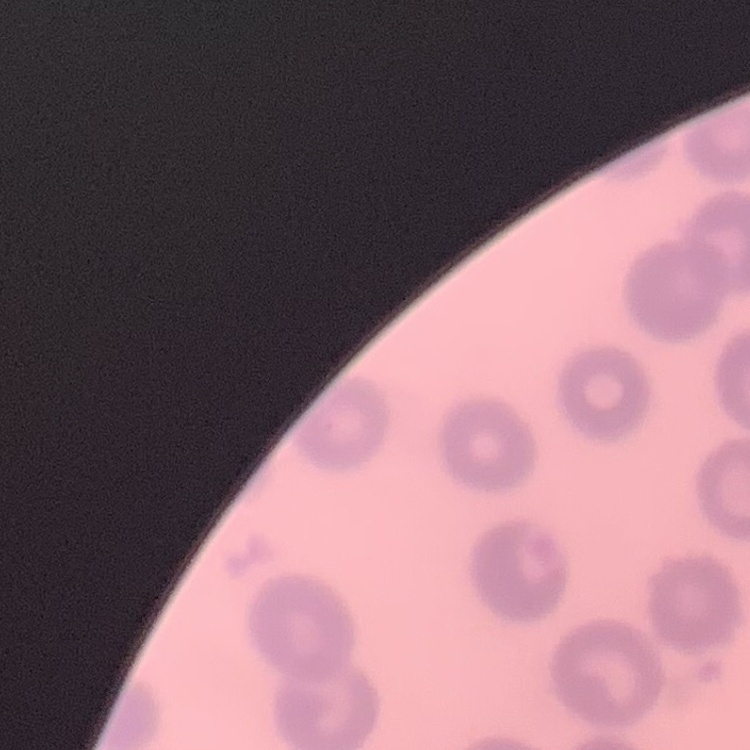
The erythrocytes show no rouleaux formation. One tile cut from a larger photomicrograph. Field's or Giemsa stain. Thin blood film.